Identify the preparation type.
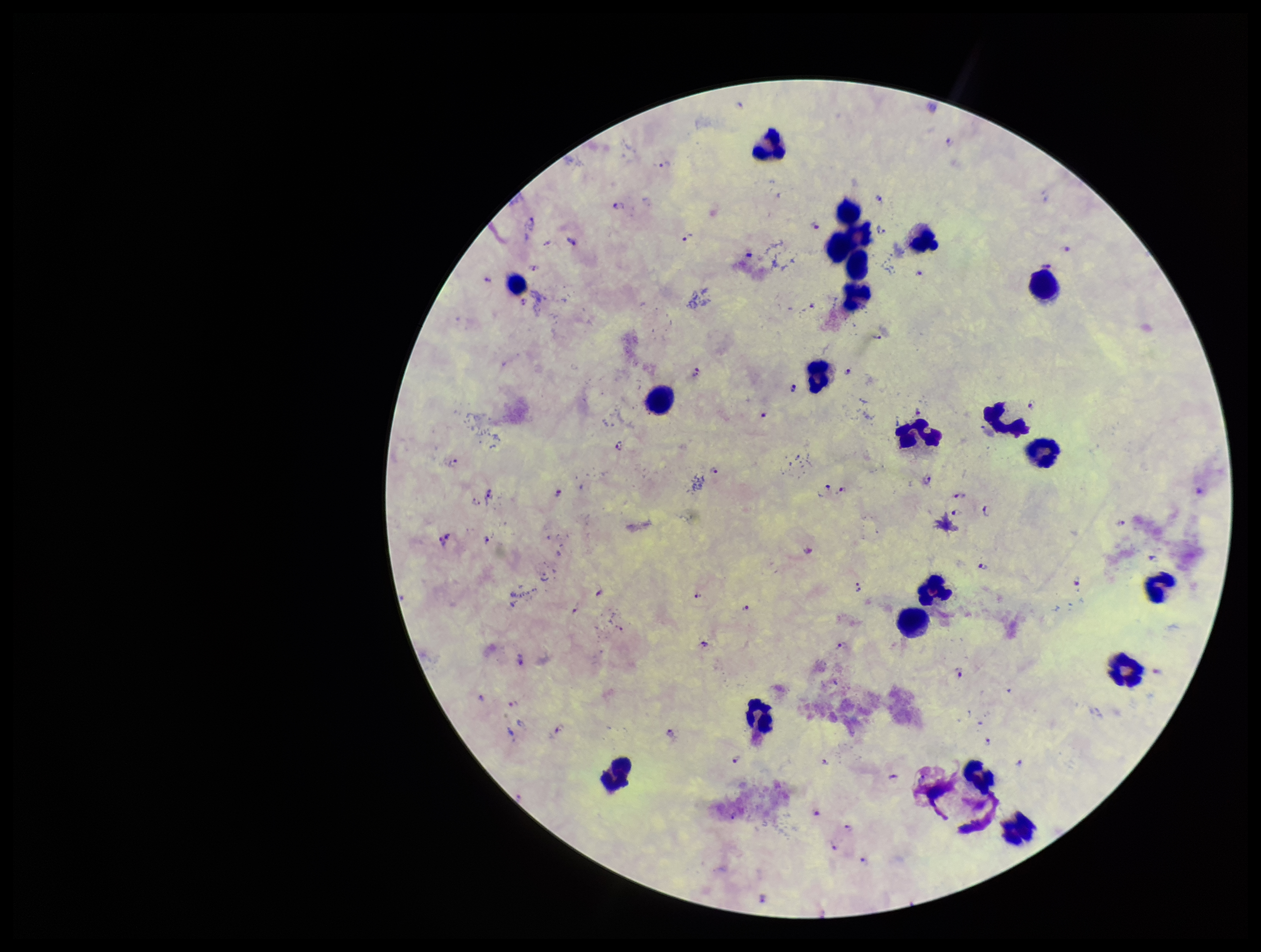
Thick.

Leukocyte count: 22. Image is 1261×952 pixels. Parasite count: 54. One field from this slide. Giemsa stain. Species reported for this patient: Plasmodium falciparum. Plasmodium parasites: detected. Smartphone photograph taken through the eyepiece of a microscope. Patient malaria status: infected.